Rate the background quality.
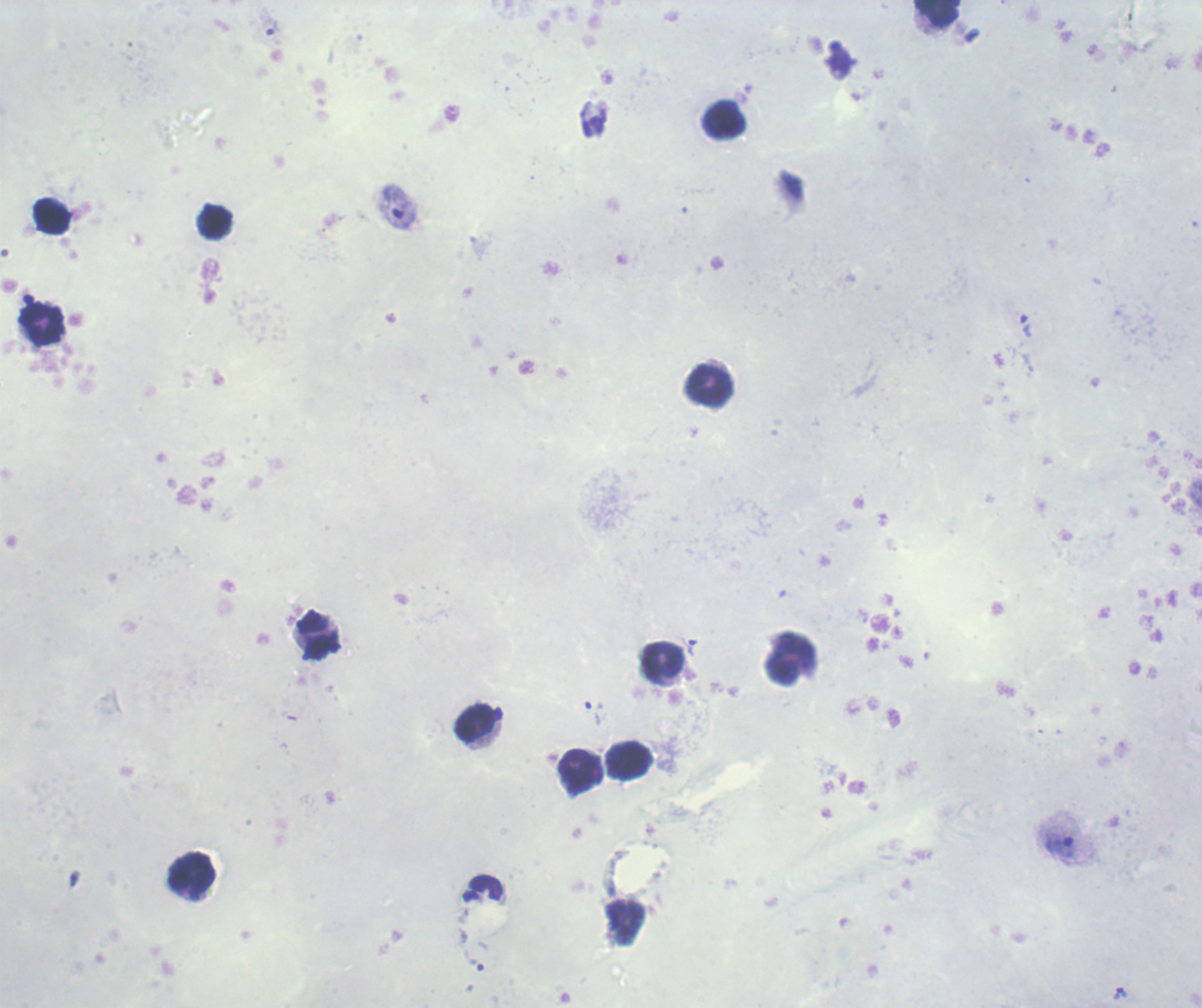

It is poor.

Approximate centers as {x, y} in pixels. Leukocyte locations: {936, 13}, {725, 120}, {51, 217}, {216, 222}, {43, 324}, {709, 384}, {317, 637}, {663, 660}, {791, 660}, {475, 725}, {628, 760}, {579, 772}, {192, 874}. Trophozoite locations: {272, 31}, {399, 207}, {1026, 327}, {693, 647}, {594, 714}, {1060, 850}, {1122, 993}. Result: Plasmodium parasites identified. Image is 1202×1008 pixels. Captured at 100x magnification. Thick blood film. One field from this slide. Romanowsky-stained preparation. Previously used in a real diagnosis.